Name the parasite shown.
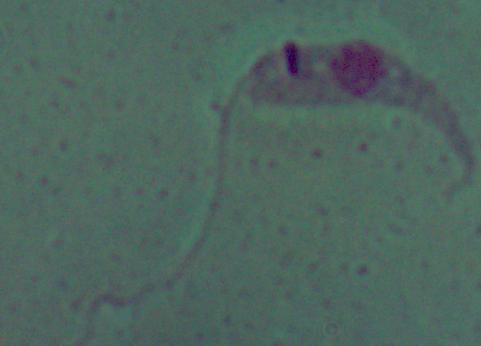
Leishmania.

magnification = 1000x
modality = micrograph